Assess this cell for malaria.
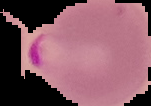

It is parasitized.

{
  "image_type": "segmented cell region on a black background",
  "image_size": "151×106 pixels",
  "preparation": "thin blood film"
}